Describe the morphology of the red blood cells.
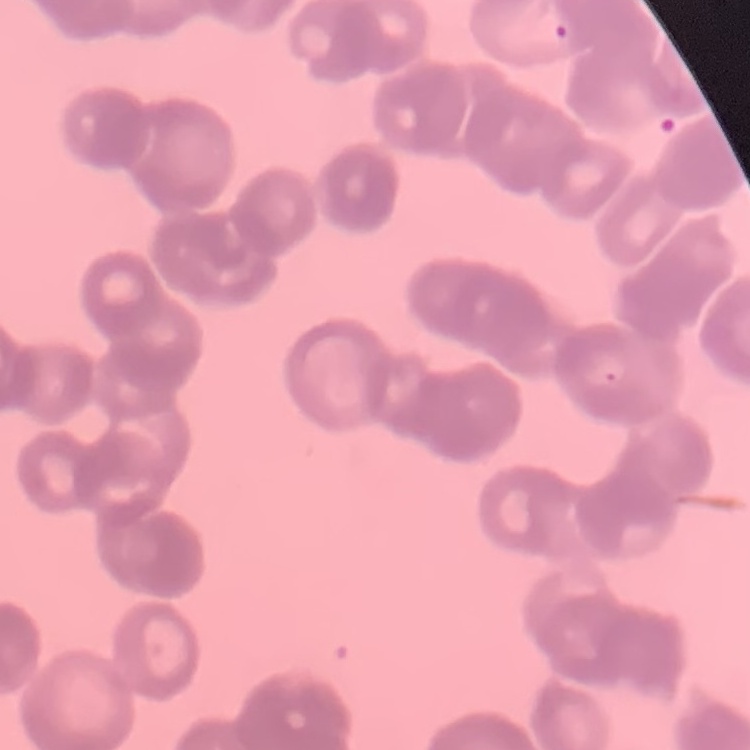
Rouleaux formation.

Summary:
  - Stain: Field's or Giemsa
  - Image type: square crop of a larger photomicrograph
  - Preparation: thin peripheral smear